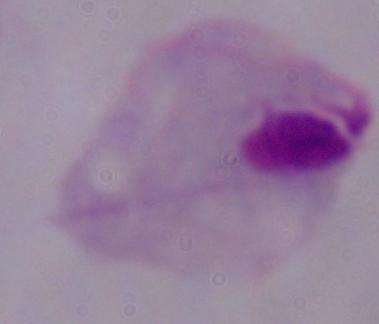
A trichomonad is shown. Photomicrograph. 1000x magnification.